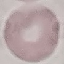 Result: negative for malaria parasites. Thin blood smear. Automatically extracted cell patch, resized to 64 × 64 pixels. Giemsa-stained preparation. Acquired by smartphone through the microscope eyepiece.